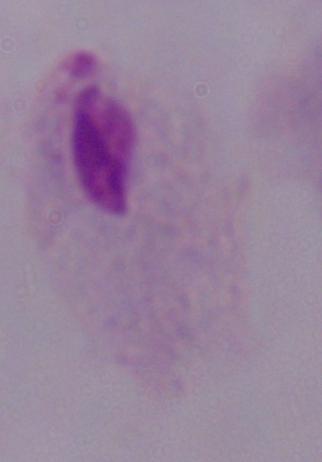
Summary:
  - Modality: photomicrograph
  - Identification: trichomonad
  - Magnification: 1000x